Outline each blood parasite and name the species.
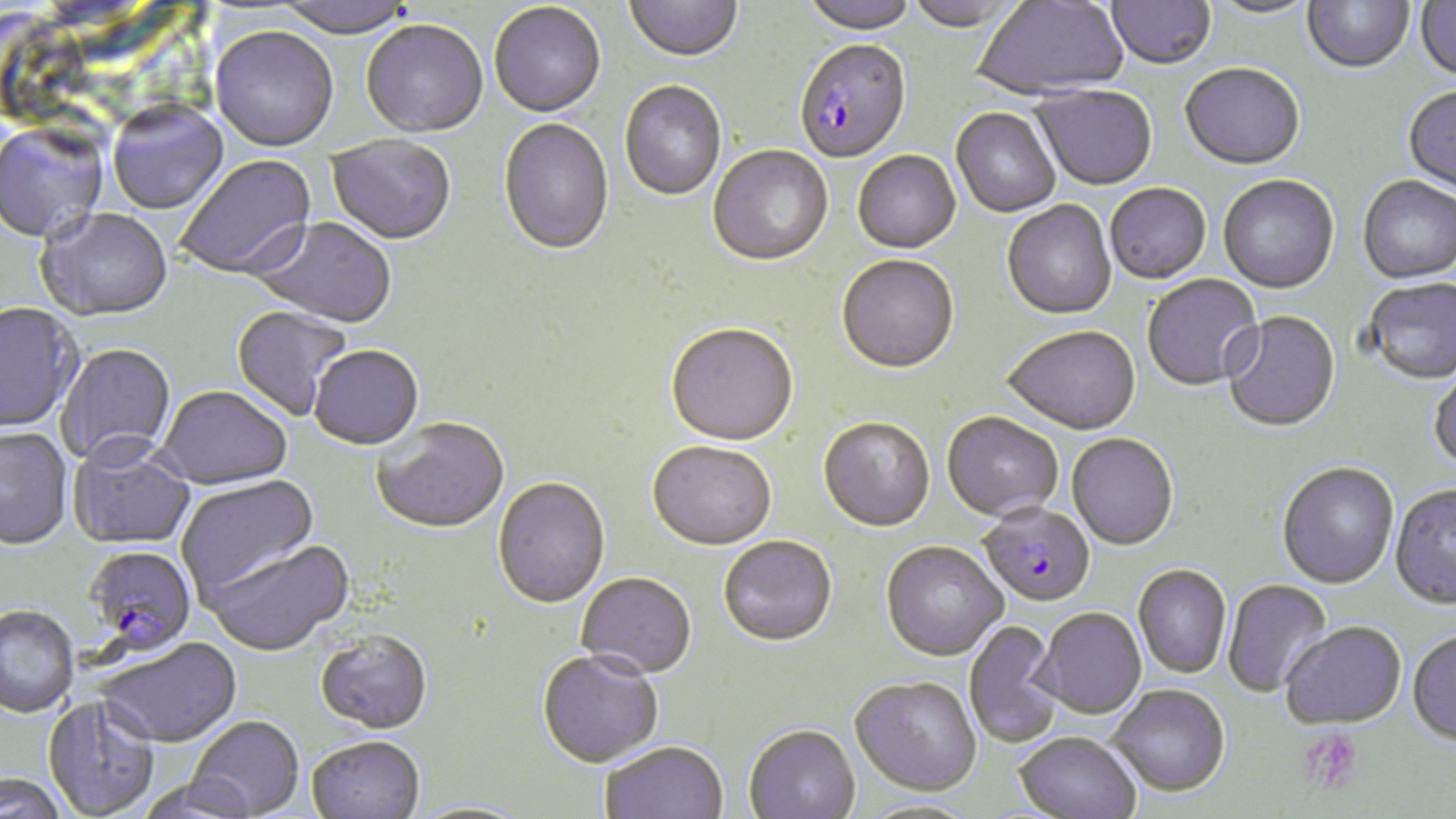
Approximate bounding boxes as [x1, y1, x2, y2] in pixels.
Plasmodium falciparum-infected red blood cells: [794, 42, 911, 165], [979, 505, 1095, 610], [82, 546, 197, 659].
No Plasmodium ovale, Plasmodium malariae, Plasmodium vivax, Babesia divergens, or Trypanosoma brucei observed.

Platelet locations: [1299, 727, 1364, 797]. Uninfected red blood cell locations: [624, 0, 743, 65], [801, 0, 916, 37], [905, 0, 1024, 34], [973, 0, 1128, 103], [1107, 0, 1216, 72], [1303, 0, 1413, 76], [1414, 0, 1456, 83], [270, 1, 416, 40], [1208, 1, 1317, 20], [488, 4, 606, 120], [361, 22, 489, 140], [210, 28, 339, 154], [1180, 65, 1305, 173], [620, 82, 726, 201], [1032, 86, 1157, 193], [1403, 87, 1456, 197], [108, 103, 229, 216], [951, 108, 1061, 218], [498, 119, 615, 258], [0, 122, 108, 245], [326, 136, 456, 247], [708, 146, 833, 268], [852, 152, 961, 256], [175, 155, 318, 282], [1218, 177, 1339, 296], [1357, 177, 1456, 286], [1105, 185, 1212, 286], [1002, 201, 1117, 322], [36, 209, 174, 324], [249, 218, 397, 330], [837, 257, 959, 376], [1142, 274, 1264, 392], [1363, 279, 1456, 387], [0, 304, 83, 434], [231, 305, 352, 422], [1221, 312, 1341, 434], [665, 325, 800, 448], [1003, 328, 1141, 437], [55, 343, 176, 469], [310, 347, 424, 452], [1427, 369, 1456, 476], [157, 387, 292, 492], [942, 413, 1063, 523], [372, 419, 509, 536], [818, 419, 935, 534], [0, 428, 74, 553], [1066, 435, 1178, 552], [67, 443, 197, 551], [647, 443, 776, 553], [1277, 464, 1399, 591], [176, 476, 321, 599], [493, 478, 610, 610], [1390, 487, 1456, 612], [718, 538, 838, 649], [202, 539, 355, 659], [880, 543, 1008, 664], [1133, 566, 1231, 679], [576, 573, 696, 682], [1222, 580, 1333, 698], [0, 607, 79, 720], [1035, 609, 1147, 720], [964, 620, 1063, 748], [1280, 624, 1407, 733], [315, 632, 433, 737], [1407, 633, 1456, 749], [94, 639, 243, 751], [536, 652, 663, 770], [849, 678, 982, 800], [1107, 687, 1230, 800], [42, 697, 160, 818], [186, 717, 305, 818], [743, 726, 861, 819], [1013, 735, 1141, 819], [306, 738, 425, 819], [600, 744, 728, 819], [1, 776, 67, 818], [135, 779, 257, 819]. Slide-level diagnosis: Plasmodium falciparum. Light microscopy. 1000x magnification. Image is 1456×819 pixels. Thin blood film. May-Grünwald-Giemsa-stained preparation. Single field of view.